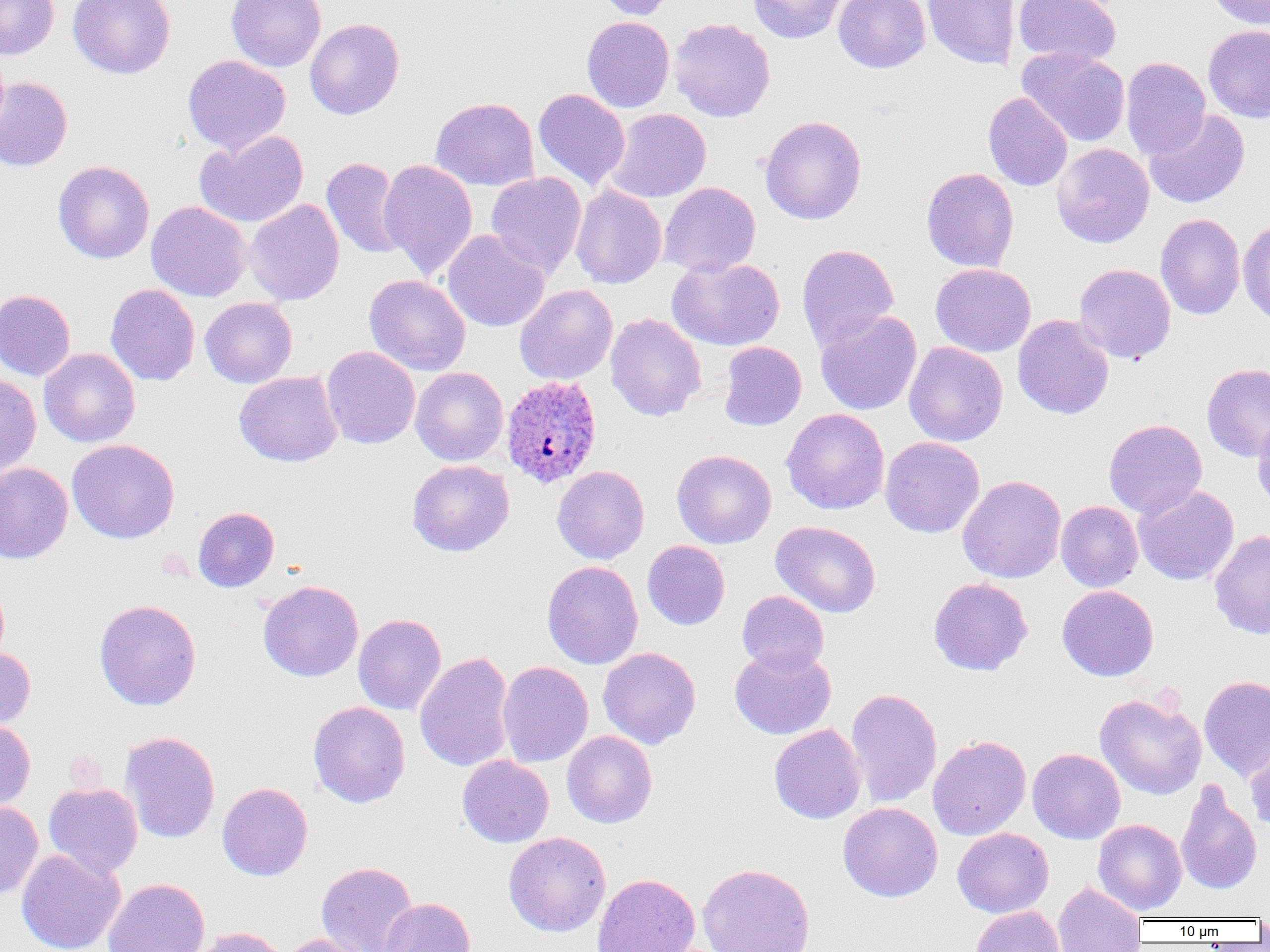
Summary:
  - Coordinate format: approximate bounding boxes as named x1/y1/x2/y2 corners in pixels
  - Uninfected red blood cell locations: (x1=0, y1=0, x2=59, y2=60), (x1=69, y1=0, x2=176, y2=79), (x1=226, y1=0, x2=326, y2=72), (x1=594, y1=0, x2=678, y2=21), (x1=747, y1=0, x2=848, y2=44), (x1=833, y1=0, x2=930, y2=73), (x1=923, y1=0, x2=1021, y2=69), (x1=1014, y1=0, x2=1121, y2=68), (x1=1205, y1=0, x2=1270, y2=31), (x1=582, y1=17, x2=674, y2=112), (x1=669, y1=18, x2=775, y2=123), (x1=305, y1=19, x2=404, y2=120), (x1=1203, y1=25, x2=1270, y2=123), (x1=1017, y1=47, x2=1130, y2=147), (x1=183, y1=55, x2=290, y2=153), (x1=1121, y1=57, x2=1211, y2=159), (x1=0, y1=76, x2=72, y2=171), (x1=533, y1=88, x2=630, y2=190), (x1=983, y1=92, x2=1072, y2=191), (x1=431, y1=97, x2=539, y2=191), (x1=606, y1=108, x2=711, y2=202), (x1=1144, y1=109, x2=1250, y2=208), (x1=759, y1=115, x2=866, y2=225), (x1=194, y1=130, x2=308, y2=228), (x1=1051, y1=143, x2=1154, y2=249), (x1=321, y1=157, x2=408, y2=259), (x1=379, y1=160, x2=478, y2=280), (x1=53, y1=161, x2=154, y2=263), (x1=921, y1=167, x2=1019, y2=272), (x1=486, y1=172, x2=587, y2=278), (x1=659, y1=182, x2=760, y2=276), (x1=570, y1=184, x2=667, y2=289), (x1=245, y1=199, x2=344, y2=306), (x1=146, y1=201, x2=252, y2=302), (x1=1155, y1=214, x2=1245, y2=319), (x1=1238, y1=221, x2=1270, y2=325), (x1=441, y1=230, x2=550, y2=332), (x1=797, y1=244, x2=899, y2=350), (x1=667, y1=256, x2=785, y2=351), (x1=931, y1=263, x2=1036, y2=357), (x1=1074, y1=263, x2=1176, y2=363), (x1=363, y1=274, x2=471, y2=376), (x1=105, y1=284, x2=200, y2=386), (x1=514, y1=284, x2=618, y2=385), (x1=0, y1=290, x2=75, y2=381), (x1=200, y1=297, x2=297, y2=388), (x1=815, y1=311, x2=922, y2=415), (x1=605, y1=313, x2=706, y2=422), (x1=1012, y1=314, x2=1114, y2=420), (x1=718, y1=341, x2=806, y2=431), (x1=904, y1=341, x2=1007, y2=447), (x1=321, y1=346, x2=420, y2=449), (x1=39, y1=348, x2=140, y2=447), (x1=1202, y1=363, x2=1270, y2=461), (x1=410, y1=367, x2=508, y2=466), (x1=234, y1=371, x2=342, y2=466), (x1=0, y1=374, x2=41, y2=477), (x1=781, y1=408, x2=889, y2=514), (x1=1252, y1=418, x2=1270, y2=509), (x1=1104, y1=419, x2=1207, y2=519), (x1=880, y1=437, x2=985, y2=538), (x1=67, y1=439, x2=179, y2=544), (x1=672, y1=450, x2=776, y2=549), (x1=407, y1=460, x2=514, y2=557), (x1=0, y1=463, x2=73, y2=563), (x1=552, y1=465, x2=649, y2=564), (x1=957, y1=475, x2=1066, y2=583), (x1=1134, y1=484, x2=1239, y2=585), (x1=1055, y1=501, x2=1143, y2=592), (x1=193, y1=507, x2=279, y2=592), (x1=770, y1=521, x2=881, y2=618), (x1=1210, y1=530, x2=1270, y2=639), (x1=642, y1=540, x2=730, y2=630), (x1=543, y1=561, x2=643, y2=669), (x1=929, y1=577, x2=1033, y2=676), (x1=0, y1=579, x2=9, y2=665), (x1=258, y1=580, x2=363, y2=681), (x1=1057, y1=585, x2=1159, y2=681), (x1=737, y1=591, x2=829, y2=674), (x1=94, y1=599, x2=201, y2=710), (x1=353, y1=614, x2=446, y2=715), (x1=729, y1=645, x2=836, y2=739), (x1=0, y1=647, x2=35, y2=730), (x1=598, y1=647, x2=701, y2=749), (x1=415, y1=652, x2=514, y2=772), (x1=497, y1=661, x2=594, y2=767), (x1=1199, y1=675, x2=1270, y2=781), (x1=846, y1=688, x2=942, y2=809), (x1=1095, y1=693, x2=1206, y2=799), (x1=308, y1=701, x2=410, y2=807), (x1=0, y1=719, x2=35, y2=812), (x1=769, y1=724, x2=866, y2=824), (x1=120, y1=731, x2=220, y2=844), (x1=562, y1=731, x2=657, y2=828), (x1=927, y1=735, x2=1031, y2=840), (x1=1245, y1=742, x2=1270, y2=834), (x1=1027, y1=748, x2=1125, y2=844), (x1=457, y1=755, x2=554, y2=848), (x1=1176, y1=780, x2=1262, y2=896), (x1=218, y1=782, x2=312, y2=881), (x1=43, y1=783, x2=143, y2=878), (x1=0, y1=800, x2=43, y2=901), (x1=838, y1=802, x2=942, y2=902), (x1=1093, y1=819, x2=1187, y2=915), (x1=952, y1=827, x2=1053, y2=918), (x1=503, y1=832, x2=611, y2=937), (x1=17, y1=849, x2=125, y2=952), (x1=316, y1=862, x2=418, y2=952), (x1=698, y1=863, x2=815, y2=952), (x1=592, y1=874, x2=700, y2=952), (x1=103, y1=878, x2=210, y2=952), (x1=1053, y1=881, x2=1147, y2=952), (x1=378, y1=897, x2=475, y2=952), (x1=969, y1=906, x2=1065, y2=952), (x1=190, y1=927, x2=288, y2=952), (x1=279, y1=934, x2=376, y2=952)
  - Plasmodium ovale-infected red blood cell locations: (x1=501, y1=375, x2=602, y2=488)
  - Slide-level diagnosis: Plasmodium ovale
  - Field of view: one of a larger specimen
  - Magnification: 1000x
  - Preparation: thin blood film
  - Modality: light microscopy
  - Image size: 1270×952 pixels